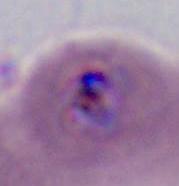
Summary:
  - Identification: Plasmodium
  - Magnification: 400x or 1000x
  - Modality: photomicrograph